Report the malaria status of this cell.
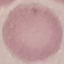
It is uninfected.

preparation = thin smear
capture = smartphone through the microscope eyepiece
stain = Giemsa
image type = automatically extracted cell patch, resized to 64 × 64 pixels